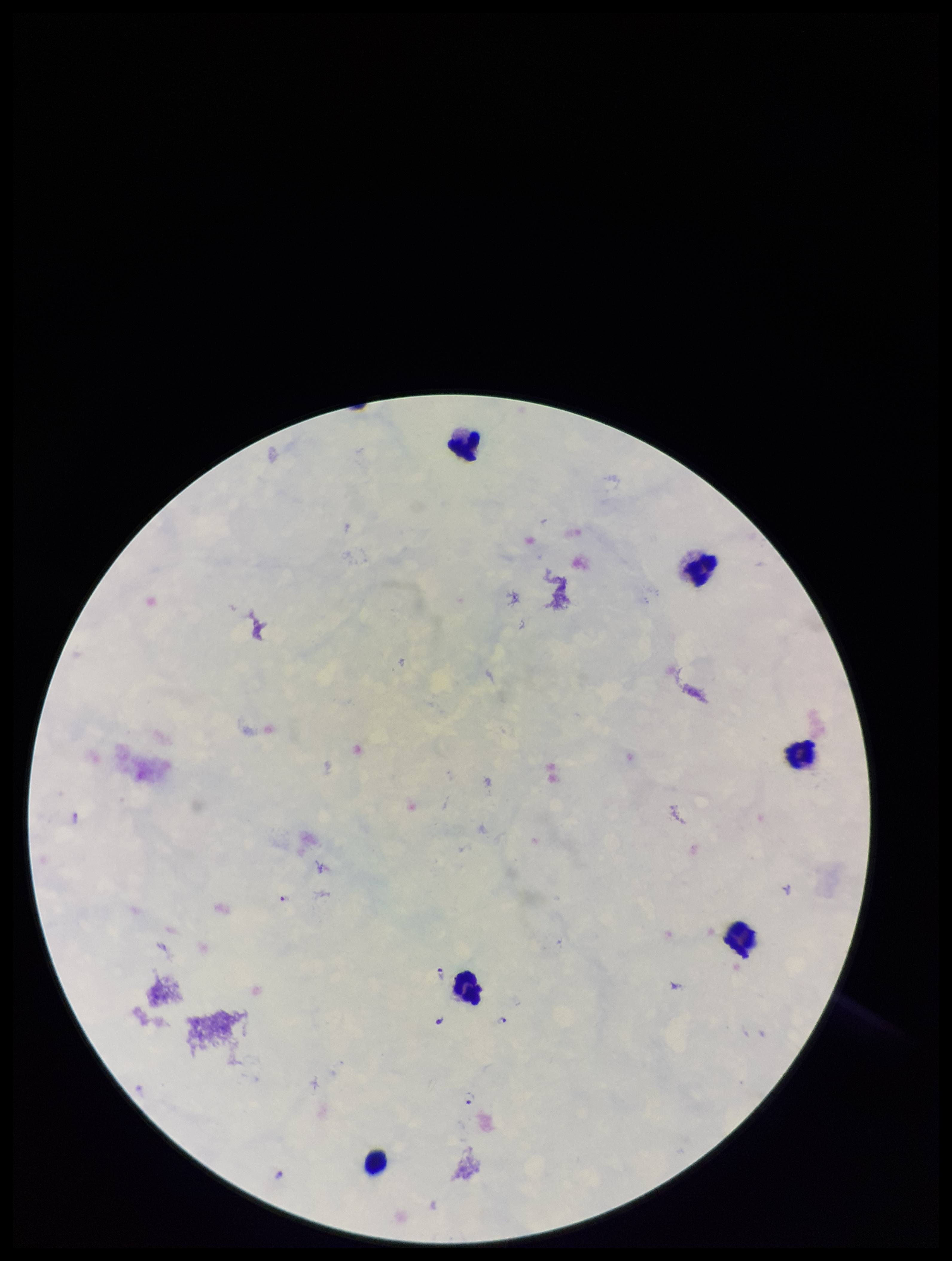
stain = Giemsa
capture = smartphone photograph through the microscope eyepiece
species reported for this patient = Plasmodium falciparum
leukocyte count = 6
image size = 952×1261 pixels
patient malaria status = infected
parasite count = 4
field of view = one from this slide
preparation = thick blood smear
Plasmodium parasites = detected